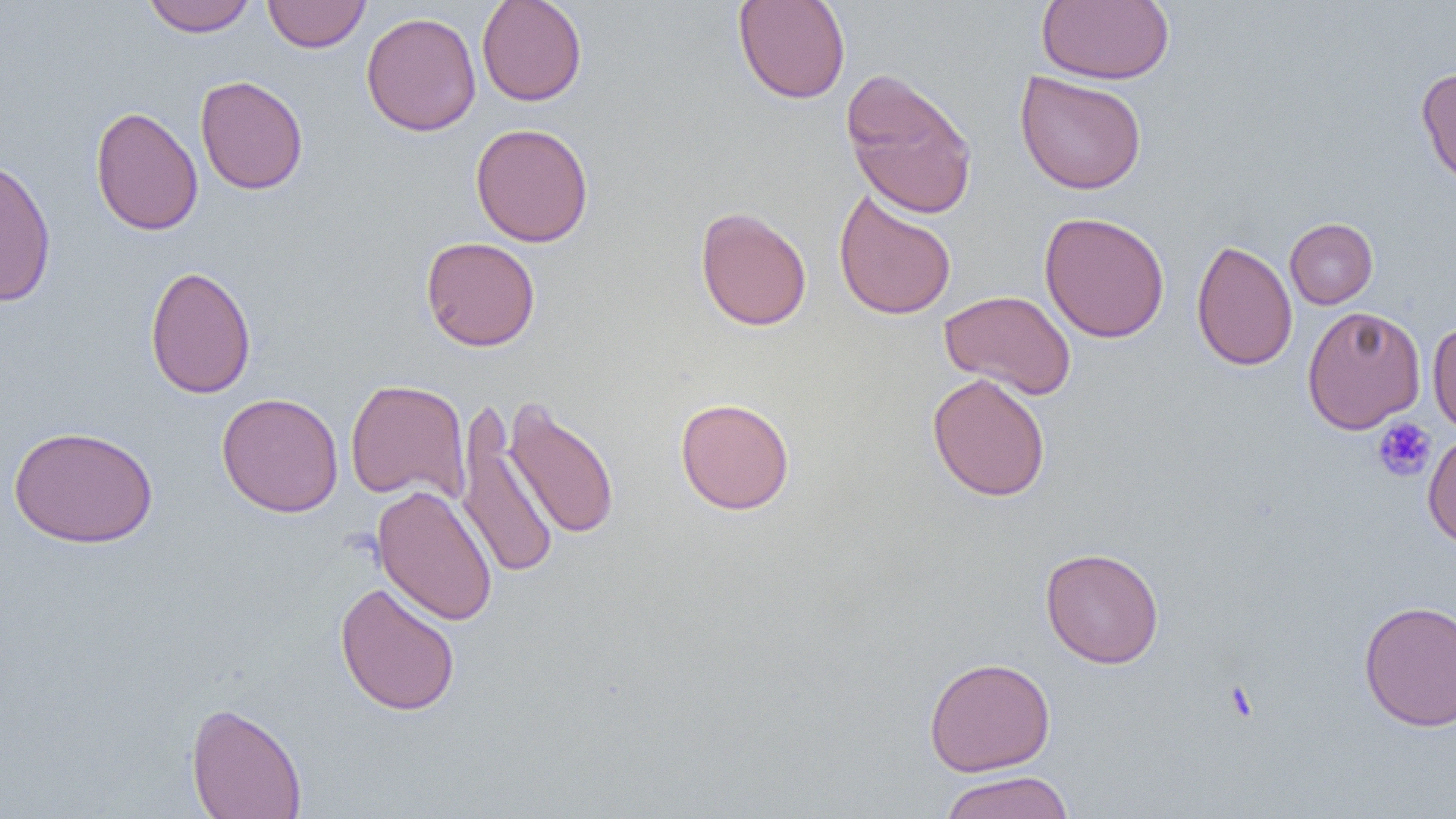
Approximate bounding boxes as (x1, y1, x2, y2) in pixels. Uninfected red blood cell locations: (142, 0, 256, 36), (262, 0, 371, 53), (476, 0, 588, 106), (733, 0, 851, 104), (1036, 0, 1174, 85), (361, 11, 481, 137), (1416, 67, 1456, 189), (840, 68, 979, 219), (1015, 70, 1147, 195), (194, 75, 309, 195), (91, 105, 203, 236), (470, 122, 593, 247), (0, 154, 57, 308), (833, 189, 957, 321), (695, 206, 812, 332), (1039, 211, 1170, 343), (1284, 218, 1378, 309), (421, 236, 541, 352), (1191, 239, 1298, 371), (144, 265, 257, 399), (939, 290, 1076, 400), (1302, 305, 1426, 433), (1428, 319, 1456, 435), (927, 372, 1051, 502), (345, 378, 471, 504), (216, 392, 344, 517), (503, 397, 620, 541), (675, 397, 795, 515), (456, 405, 559, 583), (8, 425, 159, 549), (1422, 429, 1456, 549), (372, 484, 498, 627), (1040, 547, 1164, 669), (335, 581, 461, 717), (1358, 600, 1456, 732), (924, 657, 1056, 776), (186, 701, 307, 819), (938, 770, 1075, 819). Platelet locations: (1372, 418, 1437, 482). Slide-level diagnosis: no evidence of blood parasites. 1000x magnification. Single field of view. Thin blood film. Optical microscopy. Image is 1456×819 pixels.